Give the position of every Plasmodium parasite.
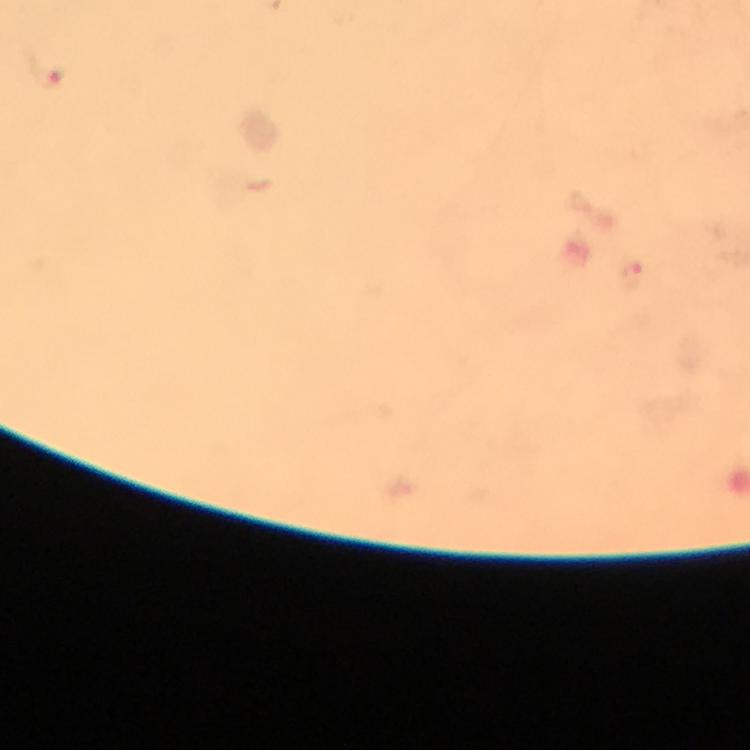
Approximate object centers, in pixels from the top-left corner.
Plasmodium parasites: (x=48, y=77), (x=630, y=275).

{
  "cropped_from": "a single field of view",
  "immersion_oil": "applied",
  "preparation": "thick smear",
  "capture": "smartphone photograph through a microscope",
  "image_size": "750×750 pixels",
  "magnification": "100x",
  "context": "from a diagnostic examination for malaria",
  "stain": "Giemsa"
}